Identify the parasite.
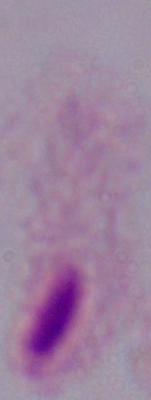

This is a trichomonad.

Captured at 1000x magnification. Photomicrograph.